Identify the parasite.
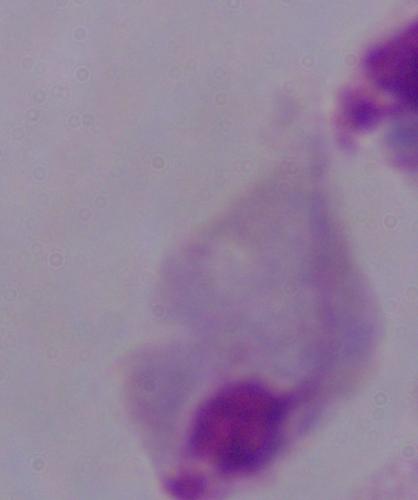
This is a trichomonad.

Micrograph. Captured at 1000x magnification.